Report the malaria status.
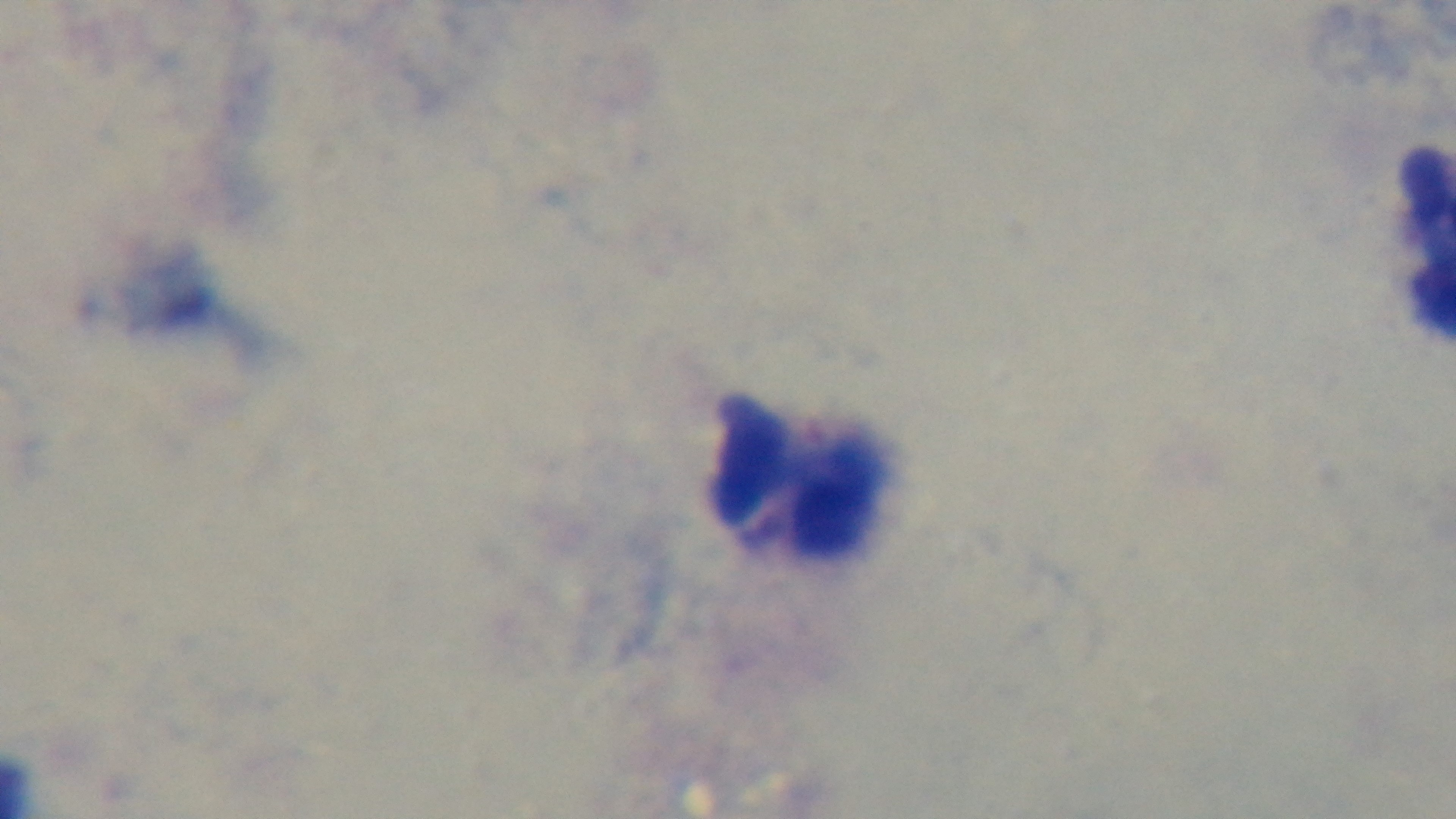
It is uninfected.

preparation: thick smear
stain: Giemsa
modality: light microscopy
capture: mounted 4K digital camera
objective: 100x oil immersion
field_of_view: single